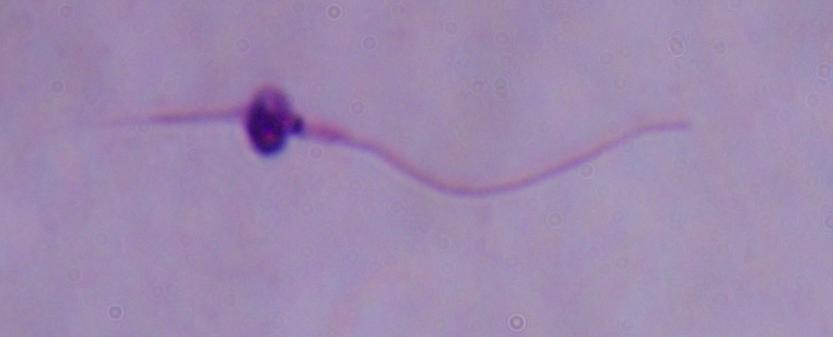
Summary:
  - Identification: Leishmania
  - Modality: photomicrograph
  - Magnification: 1000x